Outline each Plasmodium ovale-infected red blood cell.
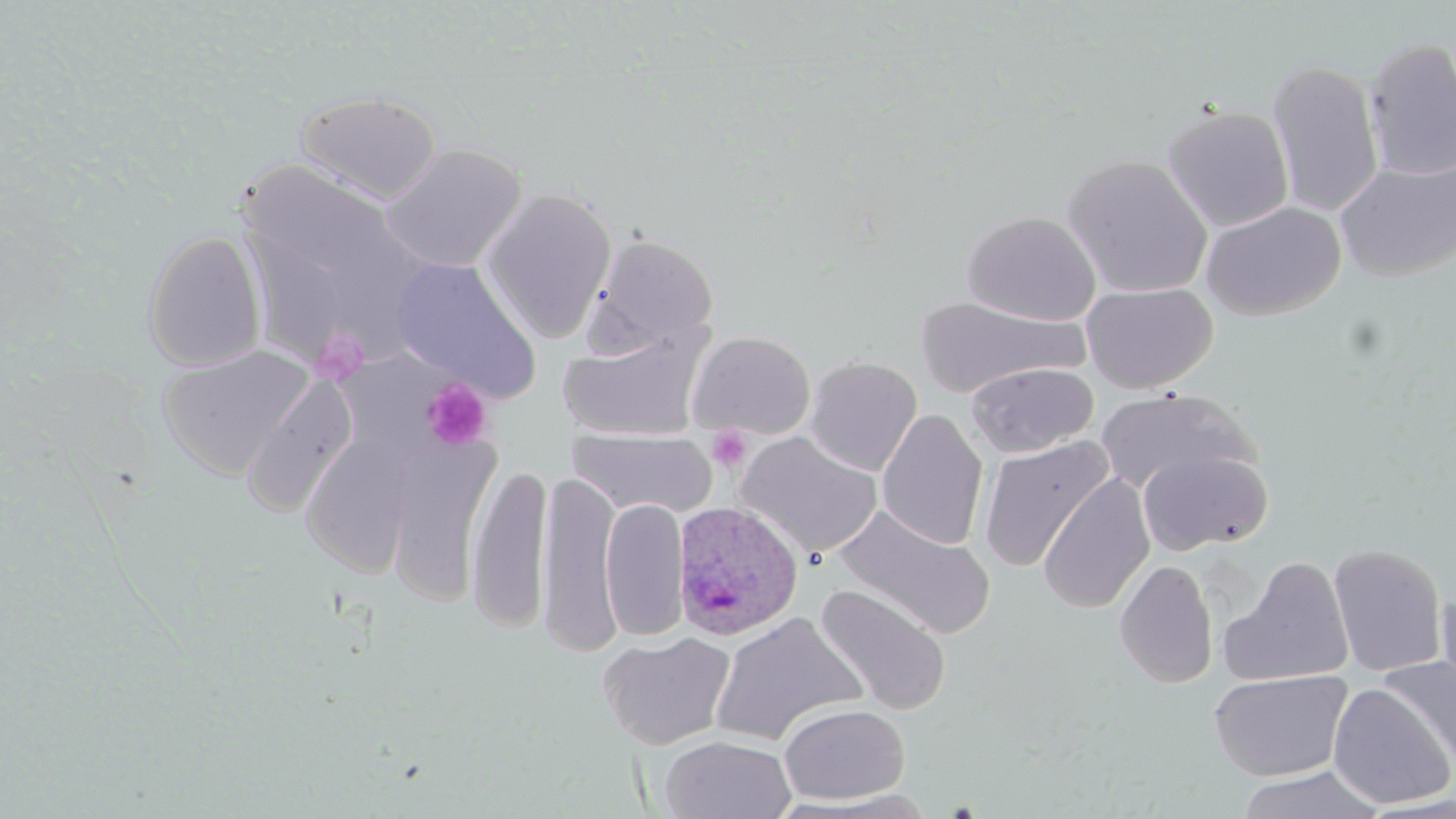

Approximate bounding boxes as (x1, y1, x2, y2) in pixels.
Plasmodium ovale-infected red blood cells: (671, 500, 805, 641).

slide-level diagnosis = Plasmodium ovale
platelet locations = approximate bounding boxes as (x1, y1, x2, y2) in pixels: (310, 327, 370, 386), (421, 378, 492, 451), (707, 425, 753, 473)
image size = 1456×819 pixels
uninfected red blood cell locations = approximate bounding boxes as (x1, y1, x2, y2) in pixels: (1363, 37, 1456, 181), (1266, 58, 1385, 218), (296, 90, 442, 204), (1162, 104, 1294, 233), (380, 142, 527, 272), (1061, 154, 1213, 299), (1335, 157, 1455, 282), (241, 164, 408, 274), (480, 188, 617, 343), (1200, 201, 1346, 321), (962, 211, 1101, 326), (141, 229, 267, 373), (586, 233, 720, 355), (391, 257, 542, 402), (1081, 281, 1218, 394), (915, 296, 1084, 398), (558, 325, 711, 443), (687, 330, 816, 440), (157, 346, 315, 479), (803, 356, 922, 477), (965, 362, 1098, 458), (241, 376, 357, 517), (1094, 387, 1260, 495), (876, 408, 989, 551), (567, 427, 718, 518), (736, 431, 883, 560), (300, 432, 418, 577), (385, 435, 501, 605), (978, 436, 1113, 574), (1137, 448, 1272, 554), (466, 463, 552, 633), (536, 469, 622, 655), (1037, 473, 1155, 614), (601, 497, 690, 642), (835, 505, 995, 639), (1328, 542, 1448, 678), (1222, 556, 1355, 687), (1114, 559, 1219, 689), (815, 584, 951, 715), (1435, 589, 1455, 703), (708, 612, 868, 746), (598, 631, 736, 750), (1379, 655, 1456, 772), (1208, 669, 1353, 781), (1328, 683, 1454, 810), (778, 703, 910, 805), (660, 734, 796, 819), (1237, 764, 1385, 819), (781, 790, 941, 818)
preparation = thin blood film
modality = optical microscopy
stain = May-Grünwald-Giemsa
field of view = one of a larger specimen
magnification = 1000x